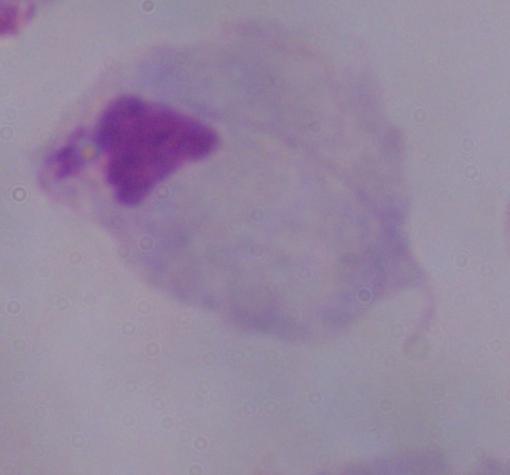
Summary:
  - Identification: trichomonad
  - Magnification: 1000x
  - Modality: micrograph